Give the extent of all uninfected red blood cells.
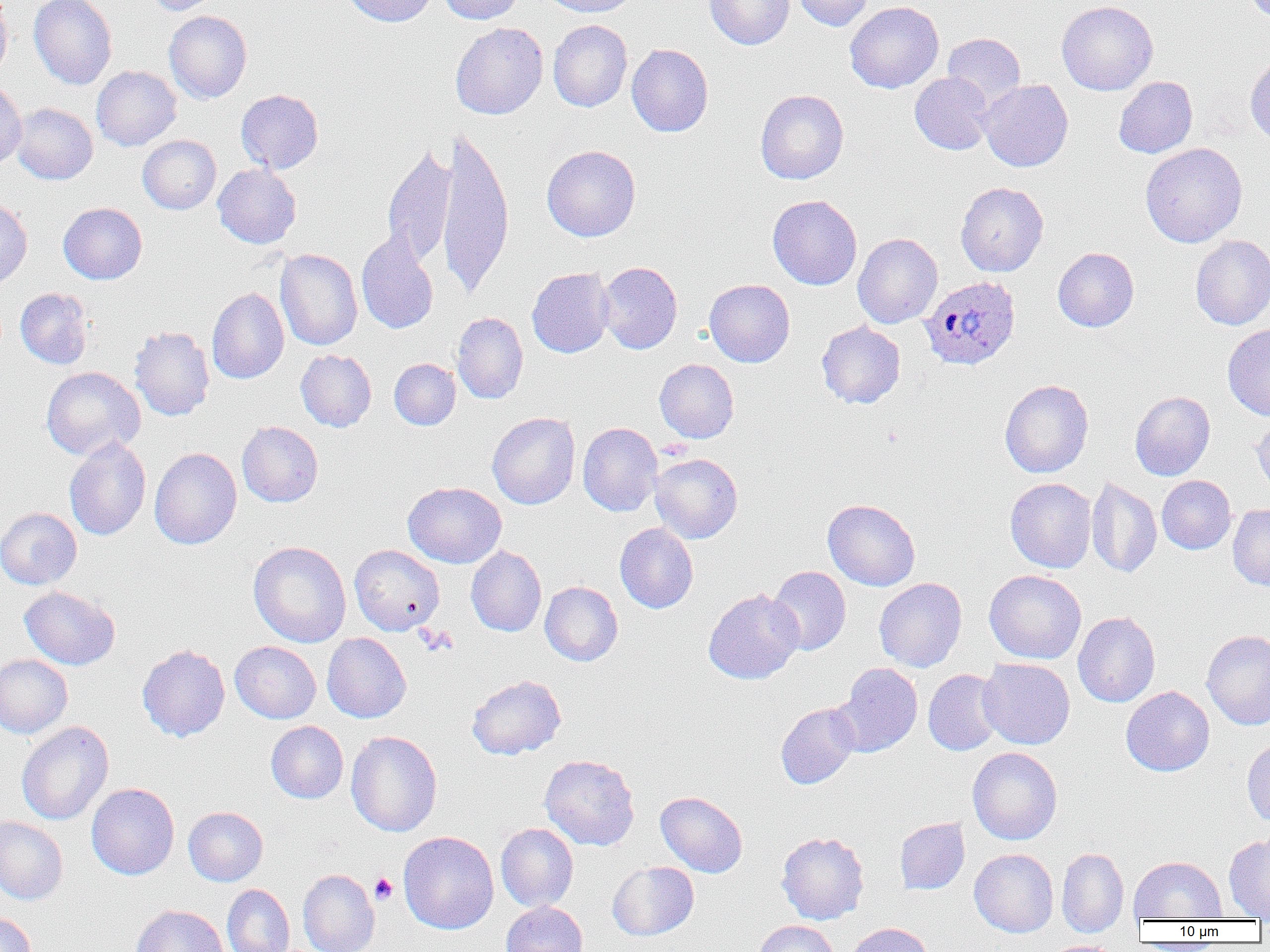
Approximate bounding boxes as (x1, y1, x2, y2) in pixels.
Uninfected red blood cells: (0, 0, 12, 83), (29, 0, 117, 90), (145, 0, 221, 15), (343, 0, 438, 27), (438, 0, 524, 25), (540, 0, 639, 17), (704, 0, 794, 49), (793, 0, 873, 31), (1244, 0, 1270, 23), (845, 1, 944, 93), (1056, 1, 1158, 95), (164, 11, 251, 104), (548, 20, 632, 112), (450, 22, 548, 119), (942, 33, 1026, 111), (626, 43, 713, 137), (1245, 53, 1270, 146), (91, 65, 182, 151), (910, 72, 994, 155), (1114, 76, 1198, 158), (0, 79, 27, 168), (978, 79, 1073, 172), (236, 89, 323, 174), (755, 89, 849, 184), (10, 103, 97, 184), (435, 130, 514, 298), (138, 135, 221, 214), (1140, 143, 1247, 247), (382, 144, 457, 268), (541, 145, 641, 242), (213, 164, 301, 248), (955, 182, 1048, 276), (767, 194, 862, 290), (0, 198, 32, 290), (58, 202, 147, 284), (356, 232, 439, 334), (853, 233, 943, 328), (1190, 235, 1270, 330), (1053, 247, 1139, 332), (275, 248, 362, 351), (596, 262, 682, 354), (527, 268, 614, 358), (704, 279, 795, 367), (15, 287, 93, 369), (206, 287, 289, 384), (451, 311, 528, 404), (816, 321, 905, 408), (129, 325, 215, 421), (1222, 325, 1270, 421), (296, 350, 376, 431), (389, 358, 460, 430), (655, 359, 739, 443), (41, 366, 145, 460), (1000, 379, 1094, 477), (1130, 391, 1215, 481), (487, 412, 580, 509), (1251, 416, 1270, 500), (237, 421, 323, 507), (577, 422, 663, 516), (64, 437, 151, 540), (149, 447, 242, 549), (650, 453, 743, 543), (1157, 475, 1236, 554), (1086, 476, 1162, 578), (1005, 478, 1096, 573), (403, 481, 506, 568), (822, 499, 920, 590), (1228, 504, 1270, 589), (0, 507, 81, 590), (614, 523, 698, 613), (249, 541, 351, 647), (349, 544, 444, 635), (465, 546, 546, 636), (768, 566, 851, 656), (984, 569, 1086, 664), (874, 578, 967, 672), (539, 581, 623, 666), (19, 586, 120, 670), (703, 588, 804, 684), (1073, 612, 1160, 707), (1202, 630, 1270, 730), (322, 633, 411, 723), (230, 641, 321, 723), (137, 644, 230, 742), (0, 654, 72, 738), (978, 657, 1075, 749), (834, 663, 922, 757), (923, 669, 1005, 756), (467, 674, 566, 759), (1121, 686, 1214, 776), (776, 703, 860, 789), (16, 721, 114, 825), (266, 721, 348, 803), (346, 730, 442, 837), (1242, 738, 1270, 827), (967, 747, 1062, 845), (540, 754, 640, 851), (86, 783, 179, 880), (655, 791, 747, 877), (184, 806, 268, 885), (0, 816, 68, 904), (894, 817, 970, 895), (496, 823, 578, 912), (398, 831, 499, 934), (776, 831, 869, 924), (1223, 834, 1270, 920), (1057, 847, 1129, 937), (969, 848, 1058, 937), (1128, 856, 1226, 922), (607, 861, 698, 941), (298, 869, 380, 952), (222, 884, 294, 952), (501, 901, 587, 952), (131, 904, 228, 952), (0, 912, 36, 952), (754, 920, 839, 952), (848, 923, 933, 952), (1041, 940, 1120, 952).

{
  "slide_level_diagnosis": "Plasmodium ovale",
  "image_size": "1270×952 pixels",
  "preparation": "thin blood smear",
  "modality": "optical microscopy",
  "magnification": "1000x",
  "field_of_view": "one of a larger specimen",
  "plasmodium_ovale_infected_red_blood_cell_locations": "approximate bounding boxes as (x1, y1, x2, y2) in pixels: (919, 276, 1020, 370)",
  "platelet_locations": "approximate bounding boxes as (x1, y1, x2, y2) in pixels: (415, 625, 458, 656), (370, 873, 398, 905)"
}